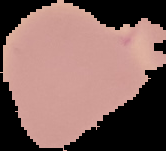

Cell region segmented out of the field of view; the surrounding area is masked to black. Image is 166×151 pixels. From a thin blood smear. Malaria status: uninfected.